Locate every Plasmodium ovale-infected red blood cell.
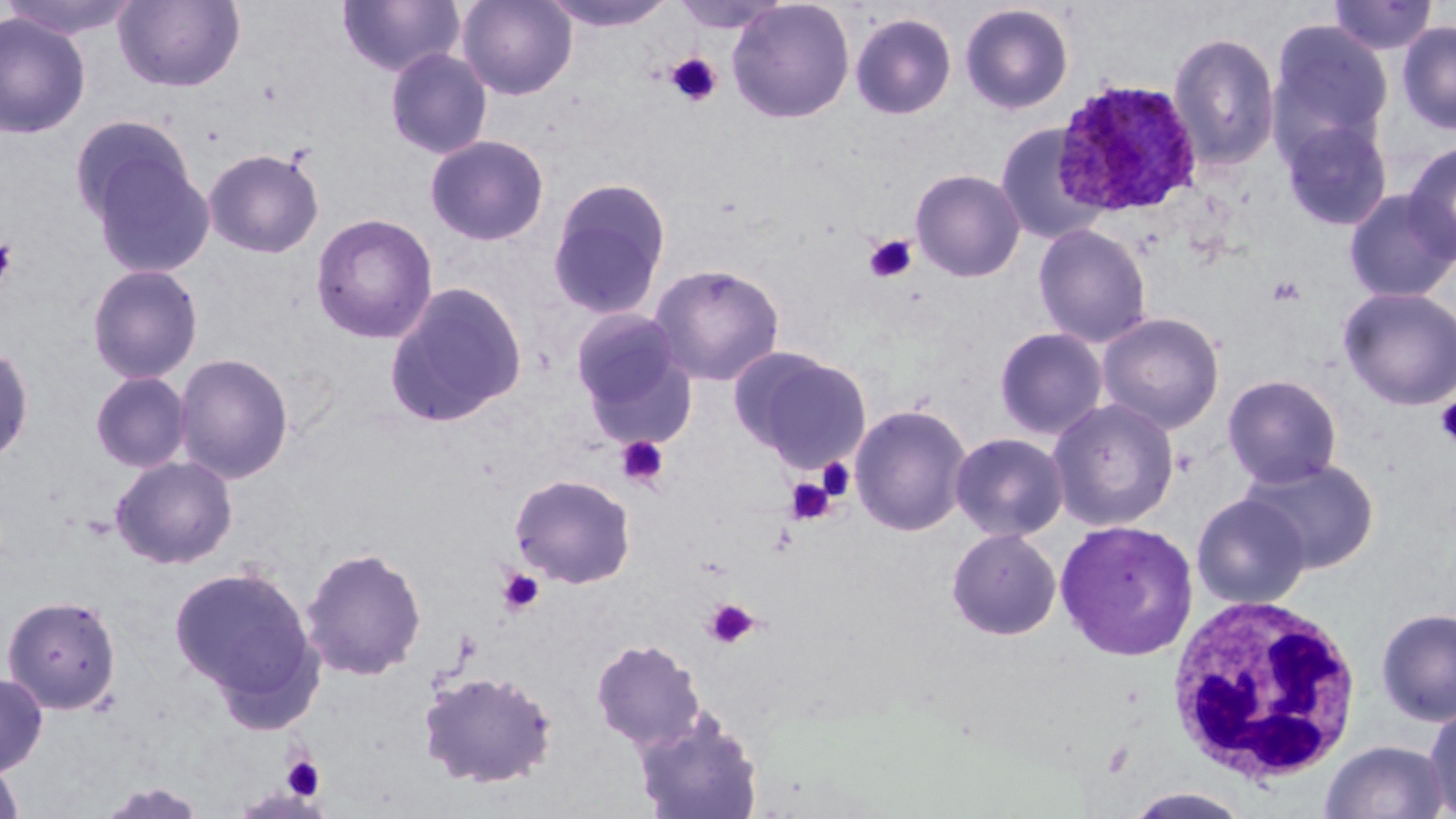

Approximate bounding boxes as named x1/y1/x2/y2 corners in pixels.
Plasmodium ovale-infected red blood cells: (x1=1053, y1=78, x2=1203, y2=217).

White blood cell locations: (x1=1164, y1=596, x2=1364, y2=785). Uninfected red blood cell locations: (x1=0, y1=0, x2=145, y2=40), (x1=113, y1=0, x2=246, y2=92), (x1=336, y1=0, x2=466, y2=78), (x1=457, y1=0, x2=577, y2=100), (x1=669, y1=0, x2=791, y2=34), (x1=727, y1=0, x2=855, y2=124), (x1=1329, y1=0, x2=1438, y2=55), (x1=542, y1=1, x2=676, y2=32), (x1=959, y1=3, x2=1074, y2=115), (x1=0, y1=12, x2=92, y2=139), (x1=850, y1=12, x2=957, y2=120), (x1=1268, y1=18, x2=1394, y2=158), (x1=1397, y1=20, x2=1456, y2=135), (x1=1168, y1=31, x2=1281, y2=171), (x1=384, y1=47, x2=493, y2=160), (x1=68, y1=114, x2=197, y2=230), (x1=1279, y1=116, x2=1393, y2=231), (x1=995, y1=124, x2=1110, y2=245), (x1=425, y1=134, x2=550, y2=246), (x1=1403, y1=141, x2=1456, y2=264), (x1=203, y1=148, x2=324, y2=258), (x1=86, y1=149, x2=216, y2=281), (x1=910, y1=169, x2=1026, y2=282), (x1=547, y1=177, x2=671, y2=320), (x1=1343, y1=189, x2=1456, y2=303), (x1=311, y1=212, x2=438, y2=344), (x1=1032, y1=223, x2=1152, y2=348), (x1=648, y1=262, x2=785, y2=387), (x1=86, y1=264, x2=204, y2=383), (x1=383, y1=282, x2=528, y2=428), (x1=1338, y1=287, x2=1456, y2=410), (x1=569, y1=306, x2=693, y2=432), (x1=1097, y1=312, x2=1225, y2=434), (x1=994, y1=327, x2=1108, y2=440), (x1=0, y1=340, x2=35, y2=467), (x1=737, y1=350, x2=873, y2=474), (x1=173, y1=352, x2=294, y2=484), (x1=89, y1=371, x2=193, y2=473), (x1=1222, y1=374, x2=1343, y2=488), (x1=1048, y1=397, x2=1179, y2=531), (x1=849, y1=403, x2=973, y2=537), (x1=950, y1=432, x2=1069, y2=542), (x1=110, y1=455, x2=238, y2=570), (x1=1240, y1=456, x2=1380, y2=573), (x1=509, y1=473, x2=637, y2=589), (x1=1191, y1=493, x2=1310, y2=609), (x1=1055, y1=519, x2=1199, y2=661), (x1=947, y1=527, x2=1062, y2=640), (x1=300, y1=546, x2=428, y2=681), (x1=169, y1=563, x2=323, y2=714), (x1=2, y1=595, x2=121, y2=714), (x1=1375, y1=607, x2=1456, y2=726), (x1=590, y1=638, x2=706, y2=749), (x1=418, y1=668, x2=558, y2=789), (x1=0, y1=671, x2=48, y2=777), (x1=1424, y1=703, x2=1456, y2=818), (x1=633, y1=708, x2=764, y2=819), (x1=1320, y1=739, x2=1451, y2=819), (x1=0, y1=757, x2=26, y2=819), (x1=1122, y1=786, x2=1255, y2=818). Platelet locations: (x1=664, y1=52, x2=722, y2=107), (x1=864, y1=235, x2=917, y2=283), (x1=0, y1=237, x2=18, y2=291), (x1=1266, y1=275, x2=1305, y2=307), (x1=1434, y1=397, x2=1456, y2=447), (x1=616, y1=435, x2=671, y2=490), (x1=816, y1=457, x2=855, y2=501), (x1=784, y1=477, x2=835, y2=527), (x1=496, y1=568, x2=544, y2=617), (x1=704, y1=599, x2=759, y2=649), (x1=282, y1=754, x2=326, y2=800). Slide-level diagnosis: Plasmodium ovale. 1000x magnification. One field of a larger specimen. Thin blood smear. May-Grünwald-Giemsa-stained preparation. Optical microscopy. Image is 1456×819 pixels.